Identify the blood parasite species.
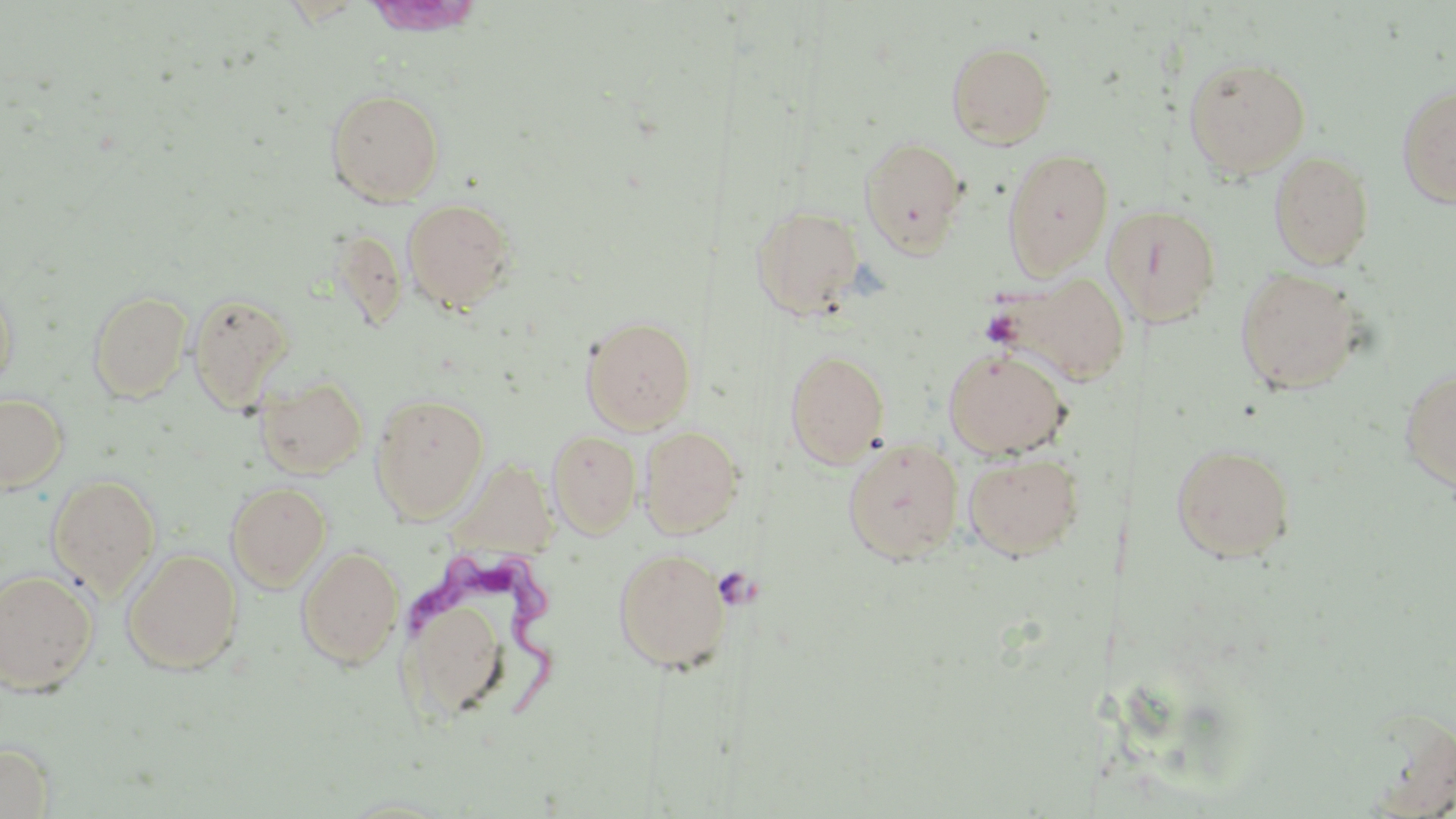
Trypanosoma brucei.

Approximate bounding boxes as [x1, y1, x2, y2] in pixels. Trypanosoma brucei locations: [410, 547, 567, 714]. Uninfected red blood cell locations: [947, 41, 1055, 148], [1183, 57, 1312, 178], [1396, 83, 1456, 209], [326, 88, 445, 206], [859, 136, 970, 258], [1002, 148, 1113, 279], [1269, 150, 1375, 270], [402, 197, 517, 313], [1104, 202, 1222, 326], [750, 204, 865, 319], [1234, 267, 1364, 395], [997, 272, 1132, 387], [0, 281, 17, 392], [88, 289, 192, 402], [188, 293, 294, 413], [581, 316, 697, 433], [942, 347, 1071, 460], [785, 349, 890, 466], [1400, 364, 1456, 495], [256, 374, 368, 479], [0, 392, 68, 492], [370, 393, 490, 522], [639, 425, 744, 538], [547, 430, 641, 538], [843, 439, 964, 563], [1170, 443, 1297, 563], [963, 452, 1085, 560], [47, 474, 161, 597], [226, 481, 331, 591], [296, 546, 404, 669], [613, 547, 731, 673], [121, 548, 242, 674], [0, 569, 98, 695], [395, 570, 525, 727], [0, 742, 54, 818], [332, 795, 465, 817]. Platelet locations: [714, 566, 759, 610]. 1000x magnification. Thin blood smear. Light microscopy. Image is 1456×819 pixels. May-Grünwald-Giemsa-stained preparation. Single field of view.